Identify the cell.
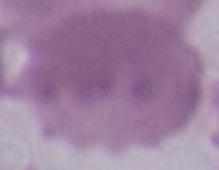

This is an erythrocyte.

Summary:
  - Modality: photomicrograph
  - Magnification: 1000x